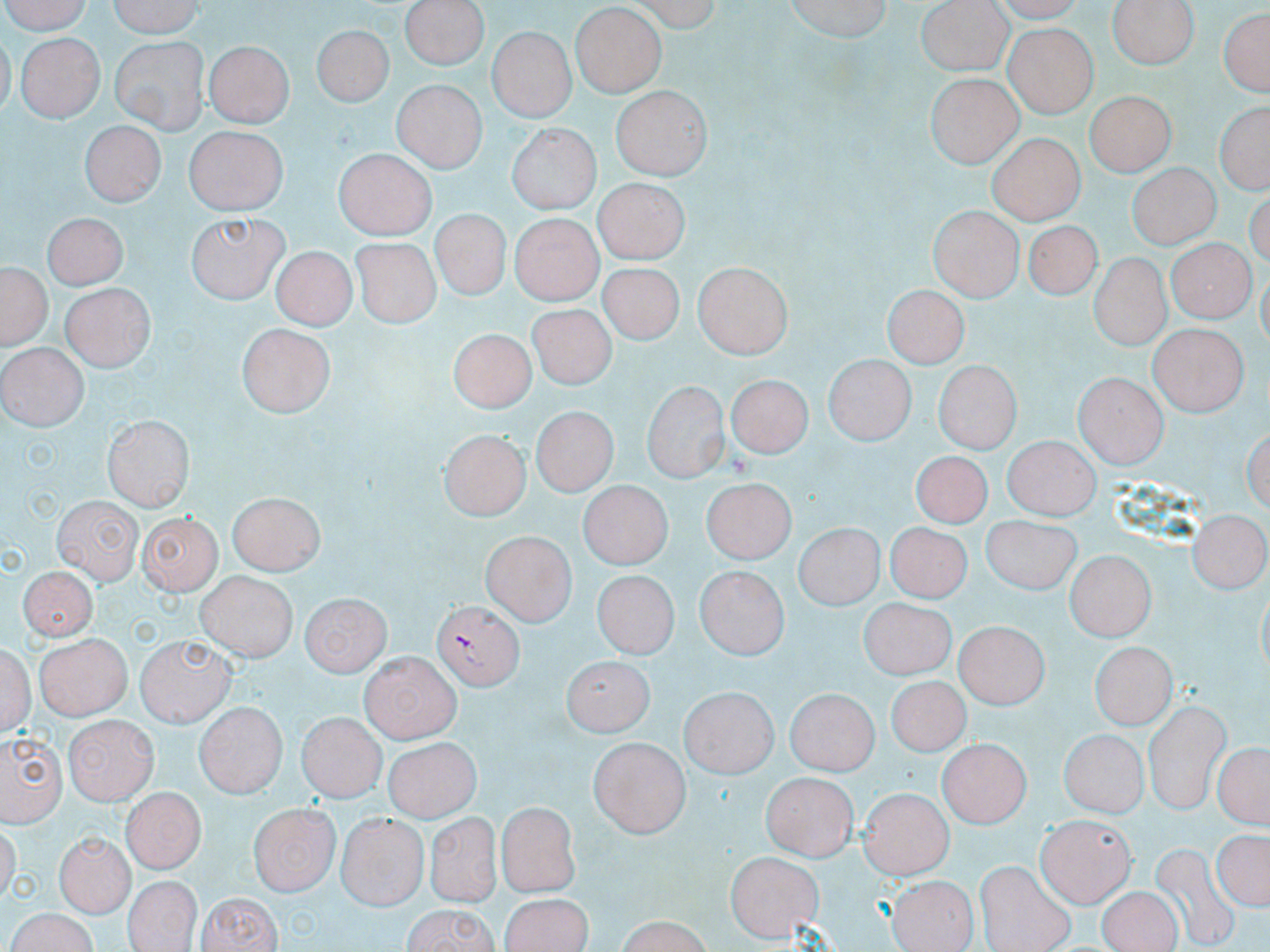

Summary:
  - Coordinate format: approximate bounding boxes as (x1, y1, x2, y2) in pixels
  - Plasmodium falciparum-infected red blood cell locations: (431, 600, 522, 691)
  - Uninfected red blood cell locations: (1, 0, 99, 34), (106, 0, 206, 37), (399, 0, 489, 70), (632, 0, 724, 32), (784, 0, 894, 44), (1107, 0, 1199, 69), (917, 4, 1013, 77), (1217, 4, 1270, 101), (572, 5, 667, 99), (7, 16, 104, 68), (311, 22, 392, 106), (1003, 25, 1094, 117), (487, 28, 575, 123), (17, 33, 103, 122), (109, 35, 208, 134), (203, 40, 292, 128), (927, 70, 1023, 167), (390, 79, 487, 171), (612, 86, 710, 178), (1087, 88, 1175, 176), (1213, 98, 1269, 197), (78, 121, 164, 208), (508, 123, 599, 213), (186, 129, 285, 216), (986, 135, 1085, 221), (333, 149, 433, 238), (1126, 165, 1221, 250), (592, 181, 687, 263), (928, 206, 1023, 298), (427, 209, 509, 301), (45, 210, 128, 287), (187, 210, 288, 304), (513, 212, 600, 306), (1028, 219, 1095, 301), (50, 231, 141, 360), (353, 238, 436, 329), (1167, 241, 1258, 322), (271, 246, 356, 328), (1087, 255, 1171, 352), (694, 263, 792, 359), (596, 264, 683, 349), (1, 265, 48, 352), (63, 284, 153, 370), (882, 286, 967, 368), (525, 305, 618, 388), (238, 323, 339, 415), (1148, 323, 1248, 416), (449, 330, 537, 417), (3, 343, 84, 431), (823, 356, 915, 447), (933, 357, 1021, 453), (1074, 371, 1165, 469), (726, 376, 809, 463), (642, 380, 731, 482), (530, 409, 615, 497), (103, 414, 194, 508), (437, 431, 527, 516), (1002, 437, 1097, 520), (911, 450, 993, 530), (702, 479, 792, 568), (579, 482, 672, 570), (231, 490, 324, 572), (53, 494, 141, 582), (980, 511, 1081, 597), (1184, 513, 1268, 599), (137, 514, 222, 594), (883, 519, 969, 601), (795, 524, 882, 610), (482, 531, 573, 625), (1064, 550, 1154, 641), (20, 562, 101, 641), (695, 565, 786, 662), (196, 570, 296, 662), (591, 572, 681, 657), (301, 592, 389, 676), (861, 595, 957, 679), (957, 621, 1050, 708), (31, 634, 131, 718), (137, 634, 234, 726), (2, 639, 36, 741), (1089, 642, 1174, 730), (360, 652, 463, 742), (564, 658, 657, 739), (885, 676, 970, 758), (676, 689, 786, 778), (784, 689, 877, 776), (194, 701, 285, 796), (297, 709, 385, 800), (67, 715, 159, 801), (0, 726, 65, 825), (1060, 730, 1147, 820), (385, 737, 479, 822), (588, 737, 687, 841), (937, 738, 1032, 827), (1212, 738, 1268, 832), (762, 769, 861, 862), (860, 788, 952, 880), (120, 790, 203, 872), (247, 802, 339, 898), (498, 802, 584, 893), (335, 809, 425, 910), (423, 810, 502, 906), (1036, 814, 1132, 905), (1210, 826, 1268, 915), (55, 829, 133, 913), (727, 849, 823, 941), (122, 875, 200, 952), (890, 876, 976, 952), (1095, 889, 1181, 952), (194, 890, 283, 952), (499, 892, 594, 950), (397, 905, 504, 952), (5, 909, 98, 952), (609, 916, 718, 950)
  - Slide-level diagnosis: Plasmodium falciparum
  - Image size: 1270×952 pixels
  - Modality: light microscopy
  - Stain: May-Grünwald-Giemsa
  - Magnification: 1000x
  - Field of view: single
  - Preparation: thin blood film